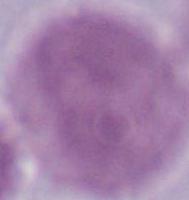
Photomicrograph. Captured at 1000x magnification. An erythrocyte is seen.